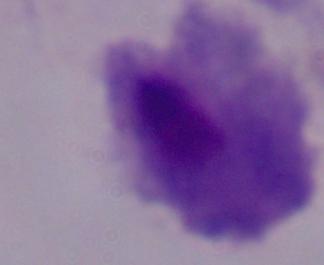

Summary:
  - Identification: trichomonad
  - Modality: photomicrograph
  - Magnification: 1000x